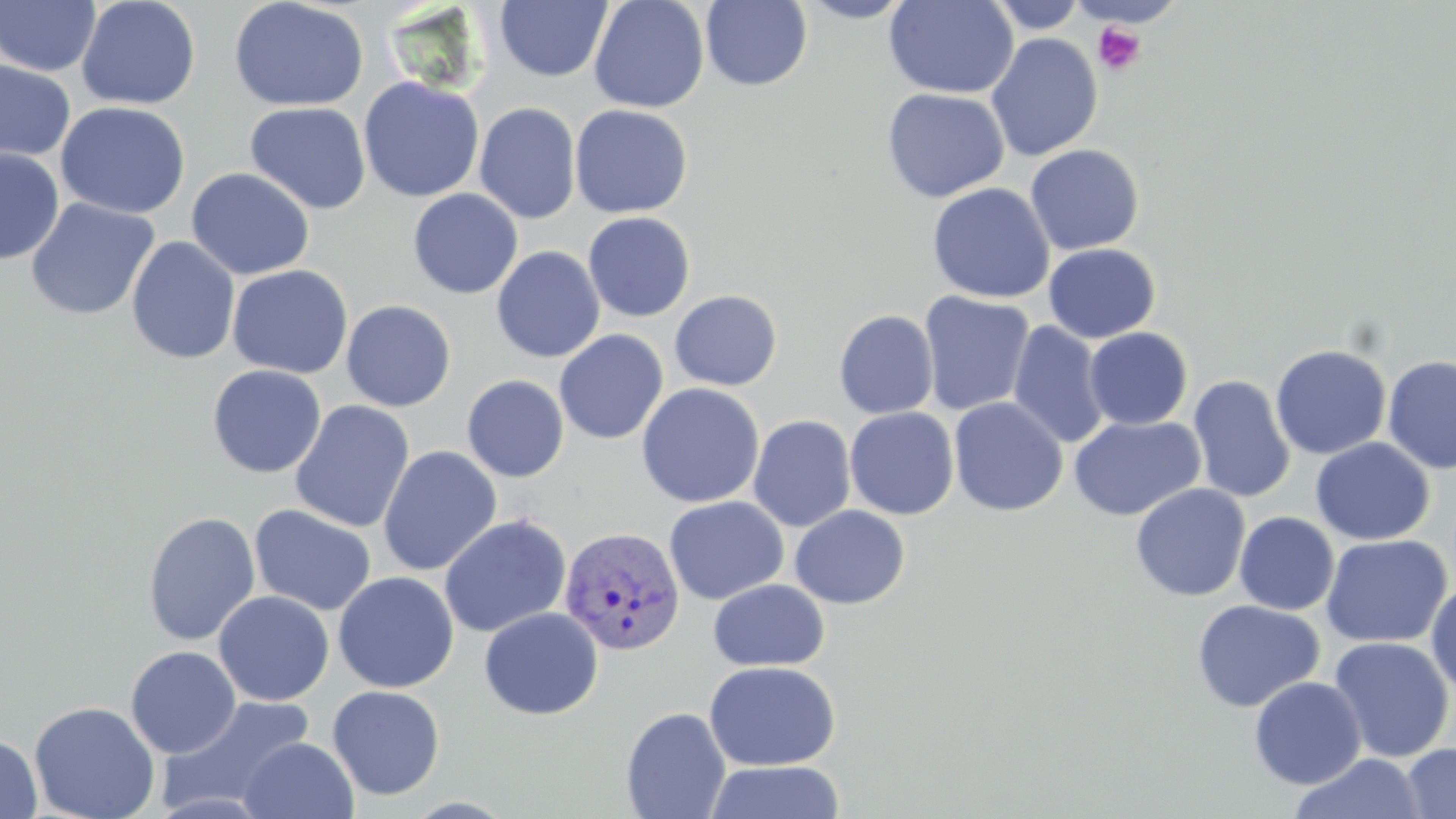

slide-level diagnosis = Plasmodium vivax
field of view = single
preparation = thin blood smear
Plasmodium vivax-infected red blood cell locations = approximate bounding boxes as named x1/y1/x2/y2 corners in pixels: (x1=559, y1=526, x2=686, y2=655)
platelet locations = approximate bounding boxes as named x1/y1/x2/y2 corners in pixels: (x1=1093, y1=22, x2=1146, y2=77)
stain = May-Grünwald-Giemsa
magnification = 1000x
uninfected red blood cell locations = approximate bounding boxes as named x1/y1/x2/y2 corners in pixels: (x1=0, y1=0, x2=101, y2=76), (x1=75, y1=0, x2=202, y2=110), (x1=228, y1=0, x2=369, y2=111), (x1=588, y1=0, x2=710, y2=113), (x1=796, y1=0, x2=917, y2=23), (x1=884, y1=0, x2=1018, y2=99), (x1=986, y1=0, x2=1090, y2=33), (x1=495, y1=1, x2=612, y2=82), (x1=700, y1=1, x2=813, y2=91), (x1=986, y1=32, x2=1103, y2=161), (x1=0, y1=60, x2=76, y2=165), (x1=358, y1=77, x2=484, y2=202), (x1=882, y1=88, x2=1010, y2=203), (x1=55, y1=101, x2=191, y2=219), (x1=245, y1=101, x2=371, y2=215), (x1=474, y1=102, x2=581, y2=224), (x1=569, y1=104, x2=693, y2=218), (x1=1025, y1=144, x2=1145, y2=255), (x1=219, y1=148, x2=363, y2=267), (x1=0, y1=149, x2=64, y2=264), (x1=186, y1=168, x2=315, y2=280), (x1=927, y1=182, x2=1054, y2=303), (x1=408, y1=188, x2=523, y2=299), (x1=25, y1=197, x2=160, y2=320), (x1=583, y1=211, x2=696, y2=322), (x1=126, y1=236, x2=241, y2=365), (x1=1043, y1=243, x2=1161, y2=343), (x1=491, y1=246, x2=605, y2=363), (x1=227, y1=265, x2=354, y2=378), (x1=669, y1=290, x2=783, y2=392), (x1=918, y1=291, x2=1035, y2=416), (x1=341, y1=300, x2=457, y2=411), (x1=833, y1=310, x2=939, y2=419), (x1=1008, y1=321, x2=1111, y2=449), (x1=1084, y1=327, x2=1194, y2=430), (x1=553, y1=330, x2=668, y2=444), (x1=1270, y1=344, x2=1392, y2=460), (x1=1383, y1=355, x2=1456, y2=474), (x1=207, y1=365, x2=327, y2=478), (x1=461, y1=375, x2=569, y2=482), (x1=1188, y1=375, x2=1296, y2=504), (x1=636, y1=383, x2=764, y2=508), (x1=948, y1=397, x2=1068, y2=517), (x1=289, y1=400, x2=415, y2=533), (x1=844, y1=407, x2=959, y2=520), (x1=748, y1=415, x2=856, y2=532), (x1=1069, y1=415, x2=1206, y2=521), (x1=1309, y1=437, x2=1435, y2=545), (x1=377, y1=445, x2=502, y2=576), (x1=1130, y1=483, x2=1250, y2=601), (x1=664, y1=496, x2=788, y2=605), (x1=249, y1=504, x2=377, y2=617), (x1=789, y1=505, x2=910, y2=609), (x1=142, y1=511, x2=261, y2=645), (x1=1234, y1=512, x2=1339, y2=615), (x1=438, y1=514, x2=572, y2=637), (x1=1321, y1=534, x2=1452, y2=647), (x1=333, y1=571, x2=459, y2=693), (x1=1426, y1=578, x2=1456, y2=701), (x1=708, y1=579, x2=830, y2=672), (x1=213, y1=590, x2=334, y2=706), (x1=1192, y1=600, x2=1325, y2=713), (x1=479, y1=607, x2=604, y2=720), (x1=1328, y1=636, x2=1454, y2=763), (x1=126, y1=646, x2=241, y2=758), (x1=704, y1=661, x2=840, y2=771), (x1=1248, y1=677, x2=1367, y2=789), (x1=327, y1=684, x2=446, y2=801), (x1=156, y1=694, x2=317, y2=815), (x1=28, y1=701, x2=160, y2=819), (x1=620, y1=707, x2=732, y2=819), (x1=0, y1=734, x2=42, y2=818), (x1=238, y1=736, x2=359, y2=819), (x1=1401, y1=743, x2=1456, y2=819), (x1=1290, y1=753, x2=1425, y2=819), (x1=704, y1=760, x2=846, y2=819)
image size = 1456×819 pixels
modality = optical microscopy